Locate the cells, classifying each as a parasitized RBC, an uninfected RBC, or a WBC.
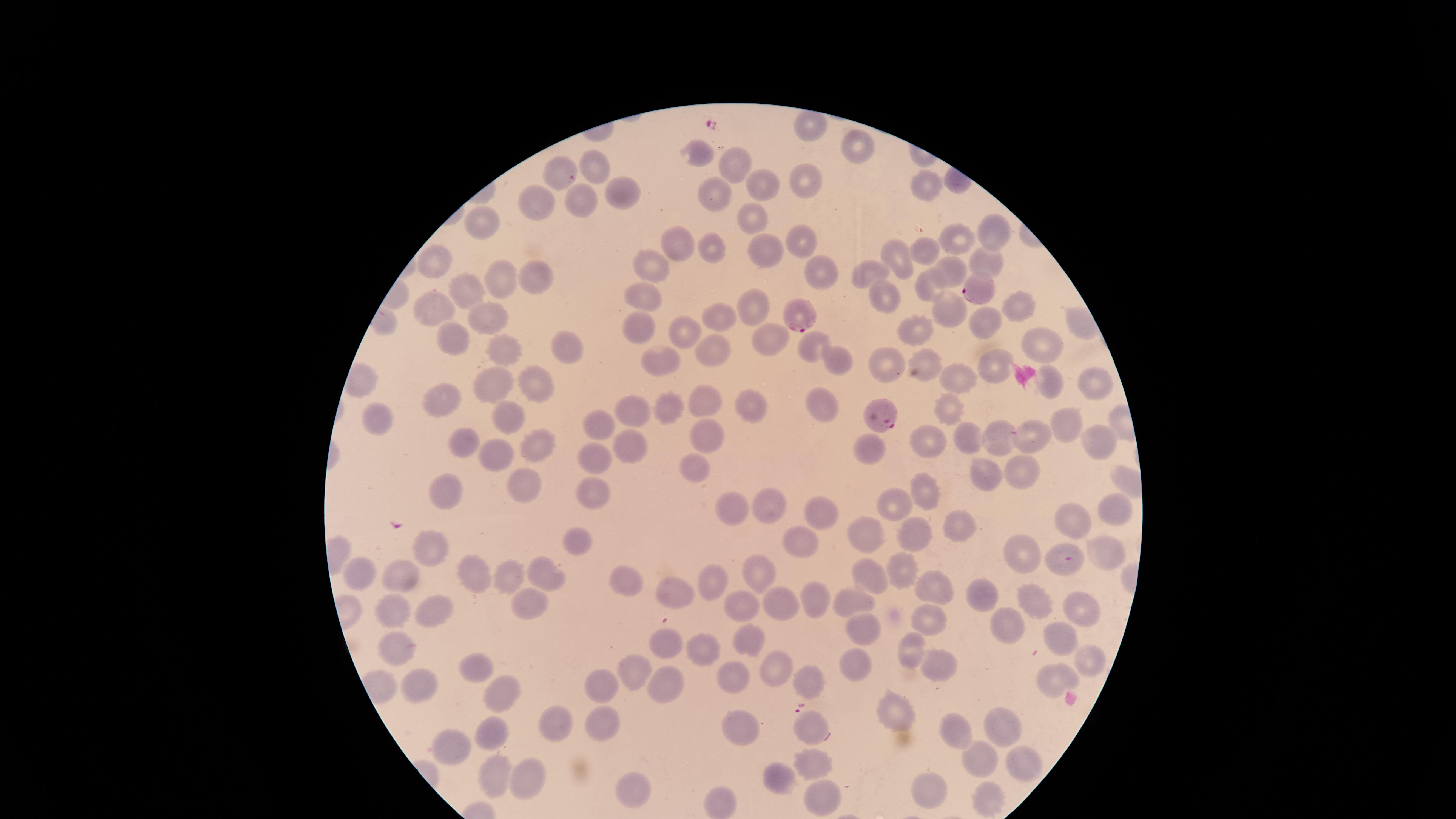
Approximate marker points, in pixels from the top-left corner.
Parasitized RBCs: (x=974, y=289), (x=800, y=318), (x=876, y=414), (x=1062, y=558).
Uninfected RBCs: (x=812, y=125), (x=854, y=148), (x=700, y=155), (x=734, y=164), (x=559, y=168), (x=604, y=168), (x=802, y=181), (x=923, y=183), (x=762, y=185), (x=716, y=193), (x=623, y=194), (x=579, y=200), (x=537, y=205), (x=476, y=214), (x=751, y=218), (x=991, y=228), (x=958, y=238), (x=805, y=240), (x=683, y=245), (x=709, y=249), (x=767, y=250), (x=898, y=251), (x=924, y=251), (x=436, y=257), (x=983, y=257), (x=648, y=263), (x=821, y=270), (x=873, y=271), (x=952, y=271), (x=497, y=277), (x=536, y=280), (x=924, y=287), (x=467, y=292), (x=642, y=293), (x=886, y=295), (x=1016, y=302), (x=753, y=304), (x=431, y=305), (x=948, y=307), (x=719, y=314), (x=486, y=315), (x=638, y=324), (x=977, y=325), (x=911, y=330), (x=683, y=334), (x=771, y=336), (x=455, y=339), (x=807, y=343), (x=502, y=344), (x=572, y=344), (x=1042, y=344), (x=713, y=351), (x=837, y=356), (x=924, y=359), (x=658, y=361), (x=886, y=362), (x=993, y=363), (x=962, y=376), (x=539, y=378), (x=494, y=380), (x=1092, y=380), (x=1053, y=382), (x=446, y=400), (x=821, y=402), (x=706, y=403), (x=755, y=403), (x=949, y=406), (x=668, y=407), (x=631, y=408), (x=505, y=412), (x=381, y=416), (x=602, y=420), (x=1065, y=422), (x=705, y=434), (x=995, y=434), (x=465, y=435), (x=967, y=437), (x=932, y=438), (x=1029, y=439), (x=1097, y=440), (x=631, y=443), (x=538, y=444), (x=495, y=450), (x=871, y=451), (x=604, y=455), (x=1026, y=468), (x=697, y=469), (x=990, y=477), (x=526, y=481), (x=920, y=486), (x=450, y=487), (x=591, y=493), (x=900, y=497), (x=767, y=503), (x=731, y=508), (x=823, y=509), (x=1117, y=510), (x=1077, y=517), (x=960, y=527), (x=919, y=534), (x=575, y=540), (x=868, y=541), (x=801, y=542), (x=1106, y=550), (x=435, y=554), (x=1027, y=554), (x=362, y=566), (x=474, y=567), (x=758, y=569), (x=904, y=574), (x=511, y=575), (x=544, y=575), (x=407, y=577), (x=873, y=578), (x=626, y=582), (x=714, y=582), (x=935, y=587), (x=676, y=594), (x=978, y=594), (x=523, y=596), (x=809, y=598), (x=1032, y=598), (x=854, y=600), (x=784, y=601), (x=1079, y=604), (x=393, y=607), (x=745, y=608), (x=439, y=610), (x=933, y=619), (x=1002, y=624), (x=869, y=625), (x=745, y=635), (x=1060, y=636), (x=663, y=639), (x=398, y=645), (x=908, y=649), (x=702, y=650), (x=1093, y=659), (x=849, y=662), (x=482, y=663), (x=776, y=664), (x=937, y=665), (x=636, y=667), (x=1055, y=678), (x=807, y=680), (x=664, y=681), (x=734, y=681), (x=421, y=687), (x=602, y=689), (x=497, y=691), (x=894, y=711), (x=608, y=718), (x=551, y=722), (x=812, y=725), (x=996, y=725), (x=950, y=728), (x=742, y=731), (x=492, y=732), (x=449, y=746), (x=977, y=753), (x=1021, y=757), (x=818, y=762), (x=491, y=768), (x=777, y=773), (x=524, y=780), (x=626, y=780), (x=926, y=791), (x=986, y=795), (x=820, y=797), (x=724, y=802).
No WBCs identified.

Summary:
  - Stain: Giemsa
  - Capture: smartphone photograph through the microscope eyepiece
  - Species: Plasmodium falciparum
  - Preparation: thin blood film
  - Field of view: single
  - Image size: 1456×819 pixels
  - Visible region: circular